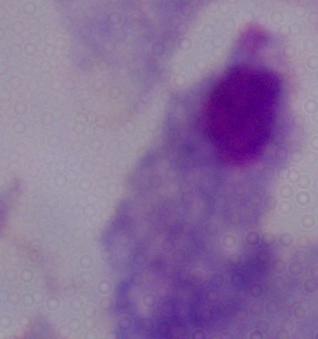

Captured at 1000x magnification. Micrograph. A trichomonad is seen.